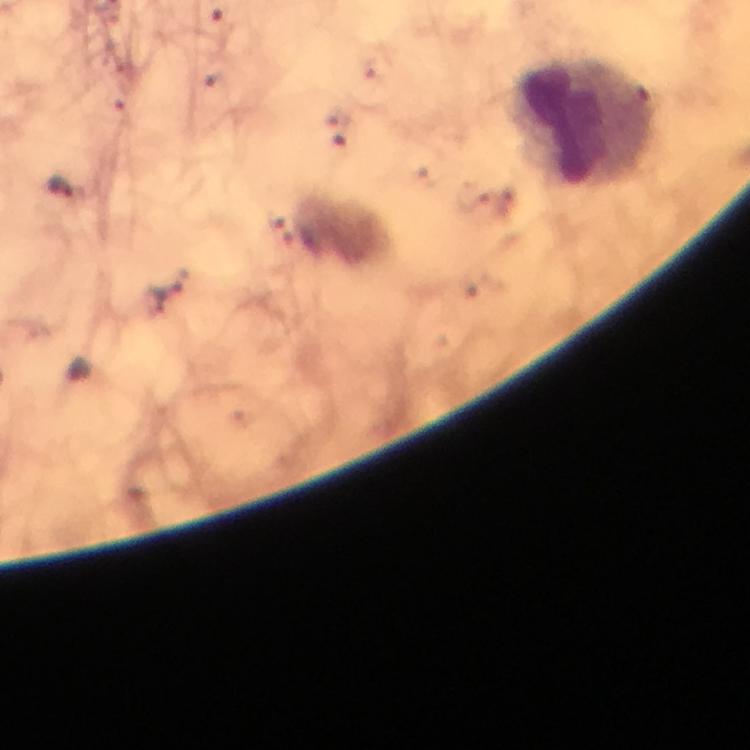

Approximate centers as (x, y) in pixels. Leukocyte locations: (583, 124). Plasmodium parasite locations: (341, 147), (59, 189). From a malaria diagnostic workup. Thick blood smear. Giemsa-stained preparation. Immersion oil applied. A crop from one field of view. Image is 750×750 pixels. 100x magnification. Smartphone photograph taken through a microscope.